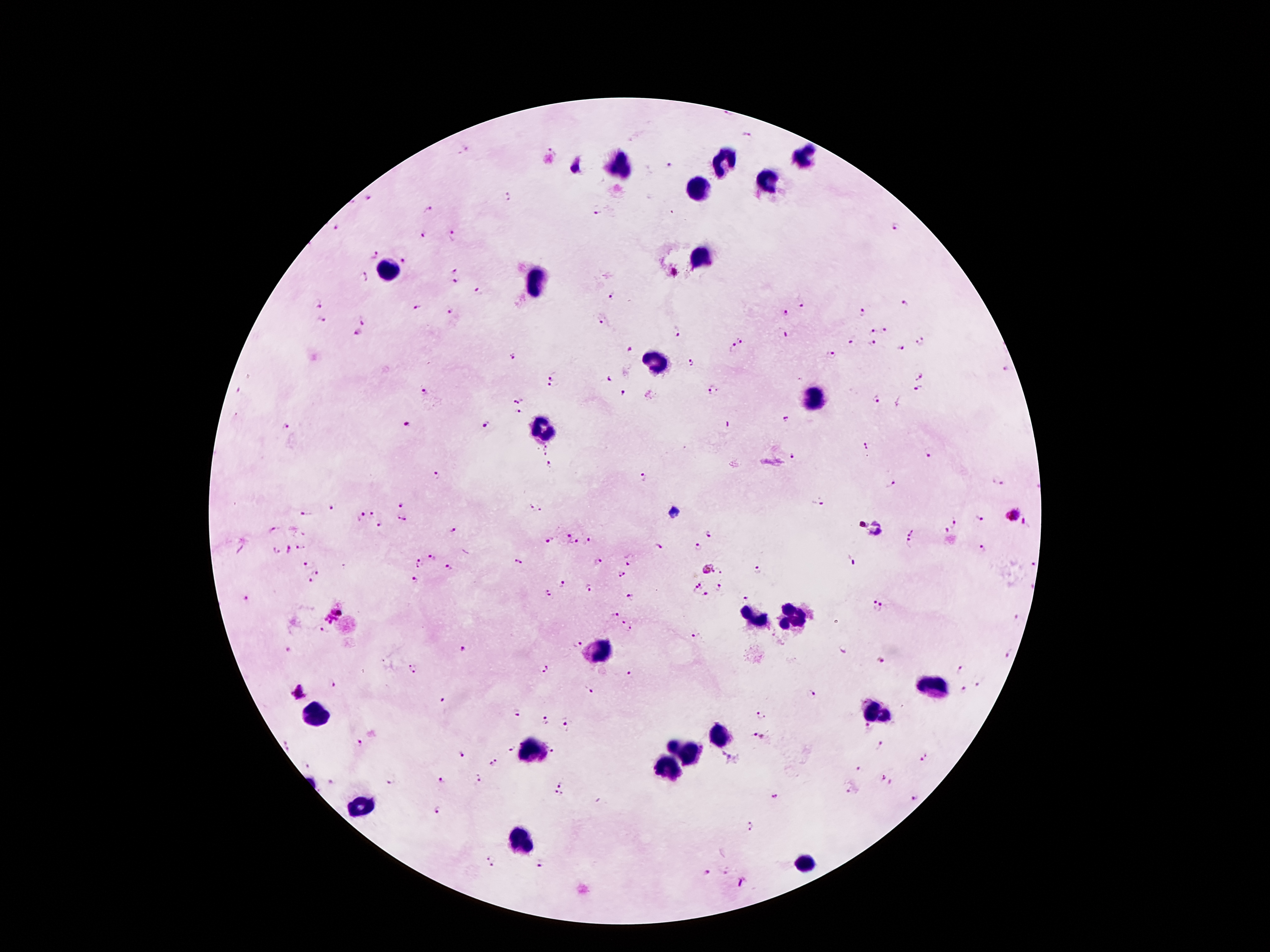
coordinate format = approximate centers as {x, y} in pixels
leukocyte locations = {804, 158}, {723, 163}, {618, 164}, {771, 178}, {702, 189}, {703, 255}, {389, 270}, {539, 278}, {656, 362}, {814, 402}, {540, 430}, {792, 617}, {749, 619}, {596, 651}, {934, 687}, {876, 713}, {318, 716}, {720, 735}, {530, 749}, {685, 751}, {664, 765}, {359, 807}, {522, 841}, {804, 863}
malaria parasite locations = {727, 114}, {748, 138}, {464, 149}, {553, 150}, {669, 166}, {509, 197}, {369, 198}, {428, 211}, {597, 211}, {897, 227}, {335, 228}, {423, 234}, {454, 234}, {374, 254}, {405, 259}, {455, 269}, {362, 277}, {456, 281}, {479, 293}, {613, 294}, {317, 301}, {801, 304}, {905, 304}, {416, 307}, {450, 312}, {786, 313}, {862, 313}, {363, 318}, {322, 320}, {602, 321}, {885, 329}, {676, 331}, {873, 332}, {356, 333}, {742, 339}, {921, 341}, {851, 342}, {872, 344}, {733, 348}, {900, 349}, {630, 350}, {831, 353}, {511, 357}, {691, 362}, {1005, 370}, {552, 374}, {919, 374}, {608, 379}, {552, 386}, {423, 389}, {715, 390}, {917, 391}, {624, 395}, {520, 398}, {875, 398}, {519, 412}, {785, 419}, {486, 424}, {407, 425}, {286, 427}, {866, 446}, {546, 448}, {928, 453}, {794, 456}, {550, 465}, {437, 472}, {643, 478}, {998, 480}, {891, 482}, {818, 501}, {402, 503}, {333, 507}, {537, 509}, {374, 513}, {305, 514}, {1015, 514}, {360, 516}, {401, 518}, {980, 519}, {957, 523}, {379, 524}, {272, 530}, {454, 530}, {912, 531}, {944, 531}, {711, 533}, {566, 536}, {589, 538}, {550, 540}, {576, 543}, {908, 544}, {302, 547}, {696, 547}, {659, 548}, {982, 548}, {288, 550}, {432, 557}, {599, 561}, {418, 562}, {518, 562}, {1031, 562}, {853, 563}, {306, 564}, {629, 564}, {708, 568}, {720, 568}, {450, 569}, {758, 571}, {318, 572}, {621, 574}, {310, 580}, {416, 581}, {704, 582}, {563, 584}, {587, 586}, {719, 587}, {691, 592}, {549, 594}, {705, 596}, {630, 598}, {246, 599}, {746, 599}, {878, 606}, {333, 610}, {612, 610}, {1018, 620}, {621, 622}, {630, 630}, {324, 631}, {695, 635}, {577, 642}, {462, 649}, {291, 650}, {1008, 653}, {880, 661}, {543, 667}, {413, 668}, {962, 669}, {630, 674}, {330, 684}, {978, 684}, {963, 689}, {589, 690}, {300, 692}, {813, 694}, {441, 698}, {518, 711}, {761, 713}, {543, 720}, {565, 726}, {869, 727}, {754, 734}, {361, 743}, {288, 746}, {512, 747}, {881, 747}, {552, 751}, {460, 753}, {923, 758}, {494, 763}, {306, 765}, {860, 768}, {883, 777}, {391, 779}, {442, 779}, {477, 780}, {332, 782}, {563, 783}, {849, 791}, {557, 793}, {774, 795}, {913, 799}, {438, 809}, {752, 826}, {491, 859}, {540, 865}, {706, 873}
preparation = thick blood film
magnification = 100x
capture = smartphone through the microscope eyepiece
field of view = one from this slide
stain = Giemsa
patient malaria status = infected with Plasmodium falciparum
image size = 1270×952 pixels